Locate every blood parasite and identify its species.
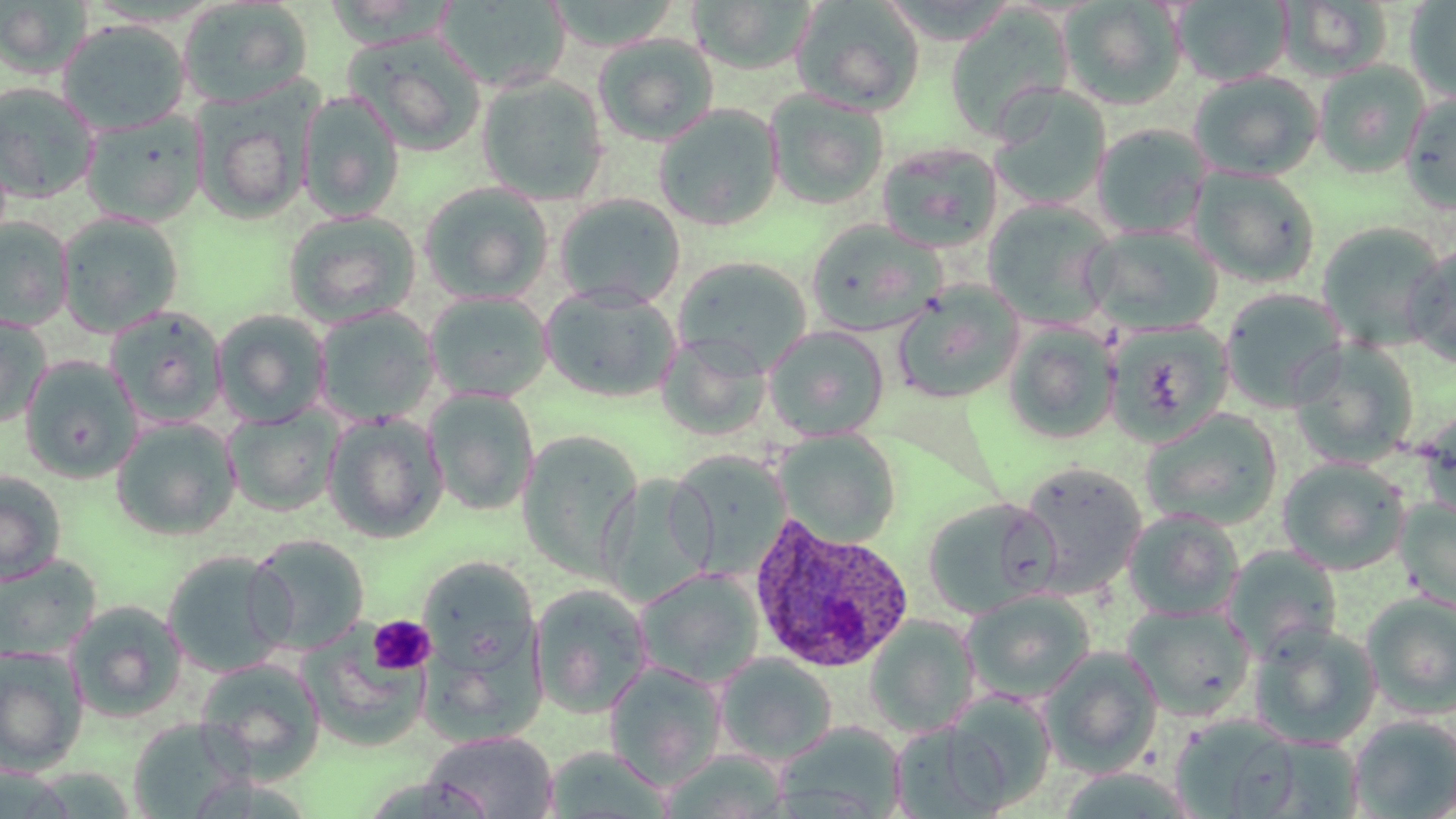

Approximate bounding boxes as [x1, y1, x2, y2] in pixels.
Plasmodium ovale-infected red blood cells: [746, 514, 914, 674].
No Plasmodium falciparum, Plasmodium malariae, Plasmodium vivax, Babesia divergens, or Trypanosoma brucei observed.

Summary:
  - Platelet locations: [368, 614, 436, 675]
  - Uninfected red blood cell locations: [435, 0, 572, 94], [542, 0, 684, 52], [790, 0, 926, 115], [1173, 0, 1293, 87], [1277, 0, 1394, 81], [1405, 0, 1456, 103], [0, 1, 92, 79], [686, 1, 821, 74], [1059, 1, 1187, 110], [178, 2, 313, 108], [944, 8, 1074, 142], [57, 19, 192, 136], [344, 32, 488, 157], [592, 33, 720, 147], [1313, 60, 1431, 179], [1188, 71, 1323, 182], [476, 73, 610, 204], [0, 82, 101, 202], [987, 85, 1112, 211], [195, 86, 312, 225], [764, 89, 889, 210], [298, 91, 405, 222], [1400, 91, 1456, 214], [653, 104, 783, 232], [79, 110, 206, 227], [1091, 124, 1212, 238], [876, 141, 1004, 253], [1188, 166, 1321, 288], [419, 181, 554, 304], [553, 193, 686, 309], [982, 199, 1117, 328], [282, 210, 422, 327], [57, 212, 185, 336], [0, 218, 74, 331], [805, 219, 947, 336], [1315, 222, 1449, 351], [1083, 223, 1224, 334], [1404, 245, 1456, 368], [672, 256, 813, 376], [892, 280, 1025, 404], [539, 284, 682, 403], [1220, 288, 1349, 411], [425, 291, 553, 403], [312, 305, 440, 427], [104, 306, 228, 428], [212, 309, 331, 426], [0, 312, 53, 428], [1105, 319, 1234, 447], [1002, 322, 1119, 444], [763, 325, 890, 441], [1289, 338, 1419, 469], [654, 342, 774, 439], [19, 356, 143, 483], [423, 388, 541, 517], [224, 405, 343, 517], [1416, 407, 1456, 523], [1140, 409, 1283, 531], [322, 412, 449, 544], [110, 418, 241, 541], [774, 428, 901, 547], [517, 430, 644, 581], [668, 452, 791, 577], [1277, 457, 1412, 575], [1017, 461, 1147, 597], [0, 471, 67, 585], [596, 474, 715, 607], [922, 498, 1057, 620], [1395, 499, 1456, 611], [1122, 509, 1245, 621], [246, 533, 370, 654], [1223, 545, 1343, 661], [162, 551, 293, 679], [0, 555, 100, 664], [418, 556, 540, 676], [634, 568, 765, 689], [530, 584, 654, 718], [962, 589, 1096, 703], [1361, 593, 1456, 717], [66, 601, 188, 722], [1122, 603, 1256, 721], [863, 615, 981, 737], [1250, 623, 1382, 750], [301, 630, 432, 751], [0, 645, 89, 775], [1039, 646, 1164, 776], [424, 649, 554, 753], [715, 653, 838, 764], [195, 657, 327, 781], [604, 662, 727, 790], [940, 691, 1057, 810], [1168, 713, 1304, 819], [1348, 714, 1456, 818], [127, 718, 250, 816], [774, 721, 907, 819], [888, 721, 1008, 818], [422, 730, 559, 818], [1245, 736, 1364, 817], [658, 751, 790, 818]
  - Slide-level diagnosis: Plasmodium ovale
  - Modality: optical microscopy
  - Field of view: single
  - Image size: 1456×819 pixels
  - Magnification: 1000x
  - Stain: May-Grünwald-Giemsa
  - Preparation: thin blood smear